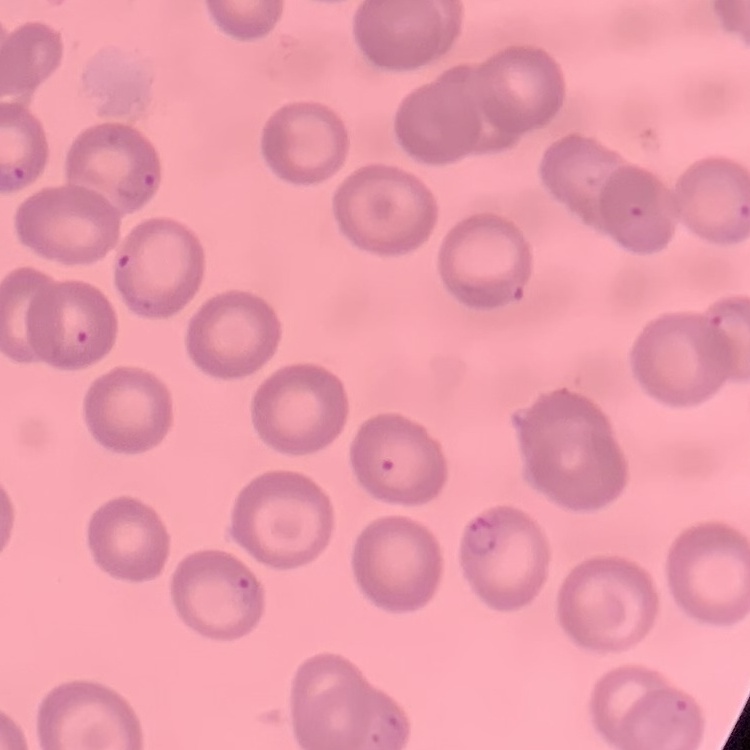

{
  "erythrocyte_morphology": "no rouleaux formation",
  "preparation": "thin blood smear",
  "stain": "Field's or Giemsa",
  "image_type": "square crop of a larger photomicrograph"
}